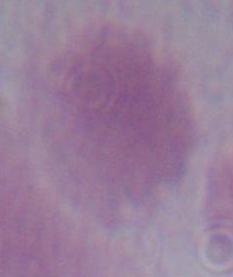

Summary:
  - Magnification: 1000x
  - Modality: micrograph
  - Identification: red blood cell